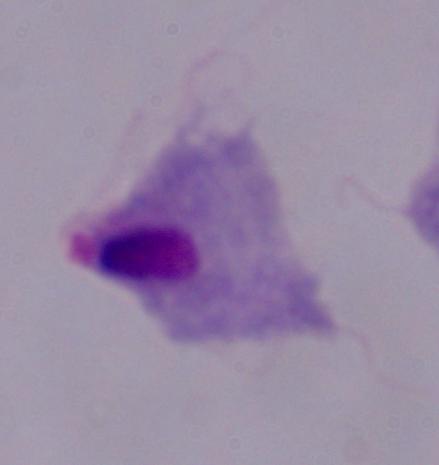

{
  "magnification": "1000x",
  "identification": "trichomonad",
  "modality": "micrograph"
}